Assess the morphology of the erythrocytes.
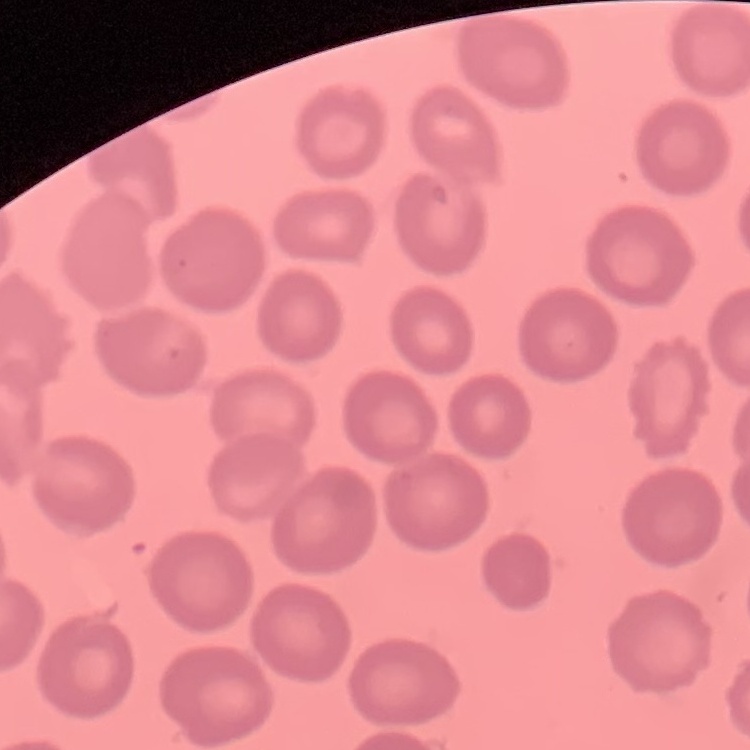

They show no rouleaux formation.

image type = square crop of a larger photomicrograph
stain = Field's or Giemsa
preparation = thin blood film